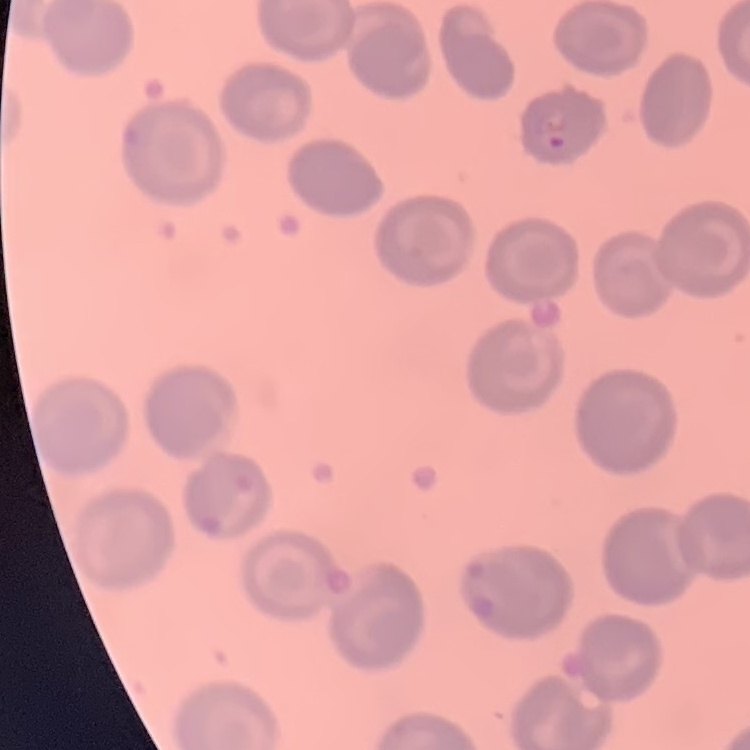

{
  "erythrocyte_morphology": "no rouleaux formation",
  "image_type": "one tile cut from a larger photomicrograph",
  "preparation": "thin blood film",
  "stain": "Field's or Giemsa"
}